Assess the morphology of the erythrocytes.
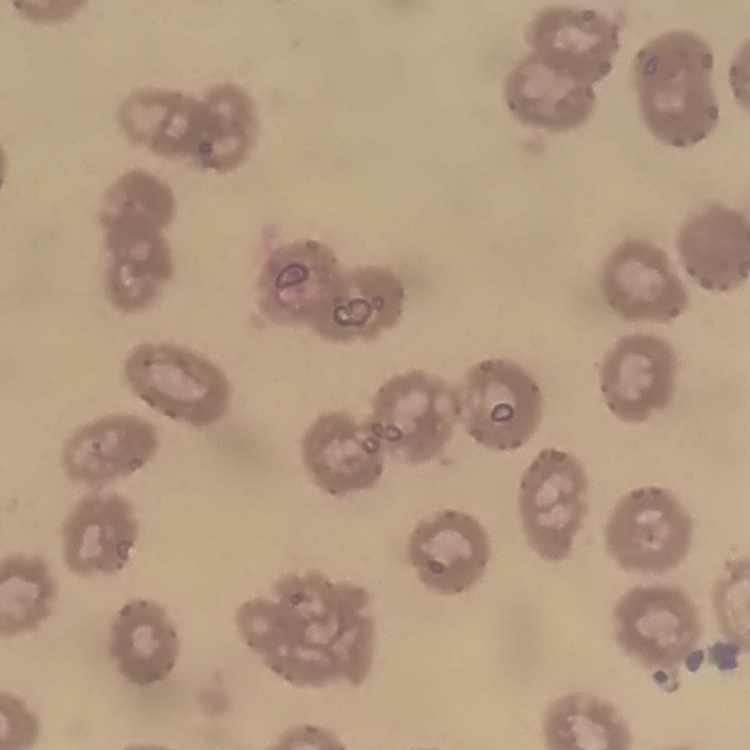

No rouleaux formation.

{
  "stain": "Field's or Giemsa",
  "image_type": "square crop of a larger photomicrograph",
  "preparation": "thin blood smear"
}